Locate every Babesia divergens-infected red blood cell.
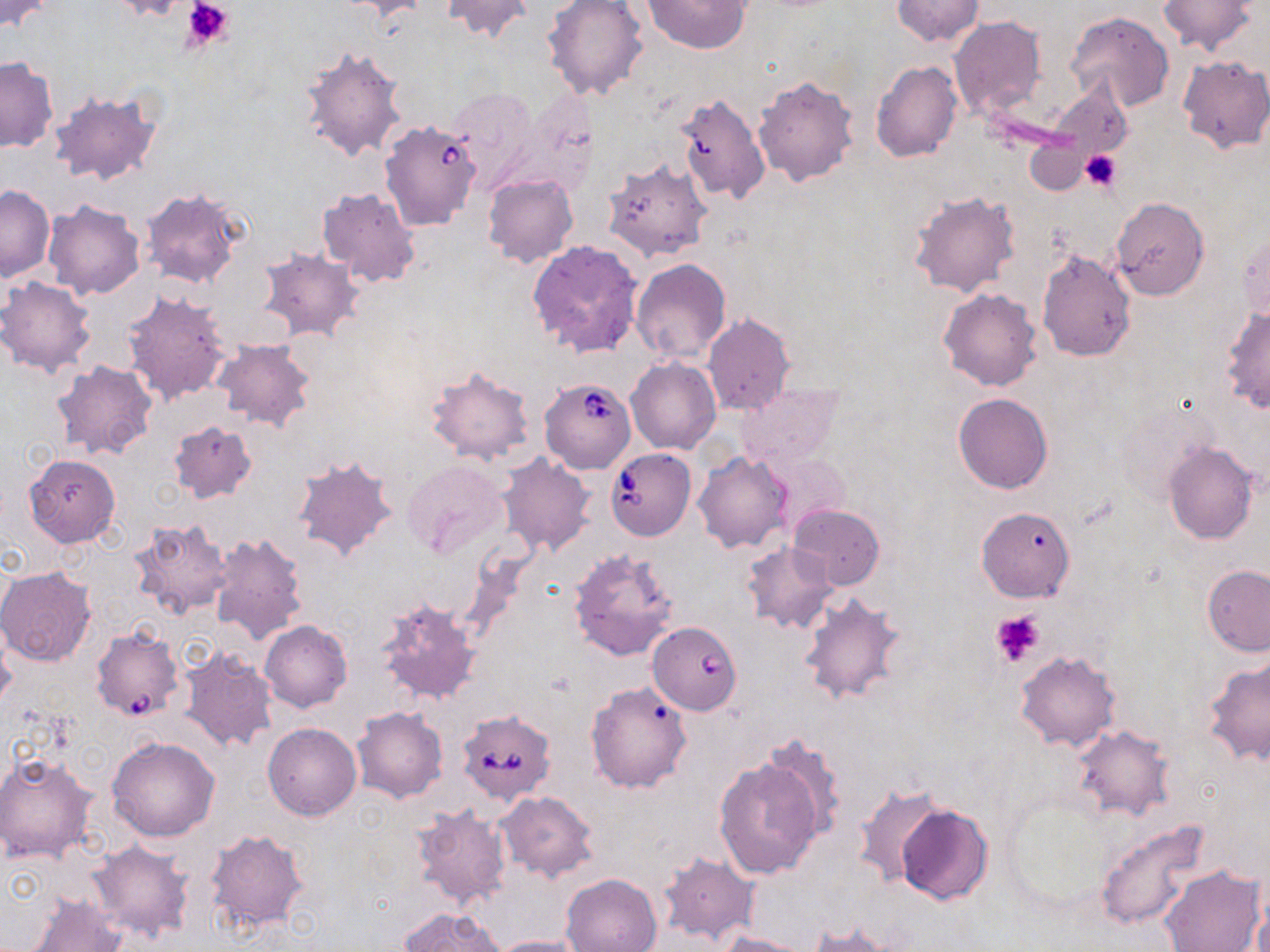

Approximate bounding boxes as (x1,y1)-(x2,y2) corner pairs in pixels.
Babesia divergens-infected red blood cells: (380,123)-(480,233), (539,378)-(636,472), (605,449)-(696,541), (648,623)-(742,722), (89,628)-(180,725), (456,710)-(556,804).

slide-level diagnosis = Babesia divergens
modality = optical microscopy
preparation = thin blood film
platelet locations = approximate bounding boxes as (x1,y1)-(x2,y2) corner pairs in pixels: (181,0)-(235,50), (1080,150)-(1121,191), (989,610)-(1045,668)
field of view = single
stain = May-Grünwald-Giemsa
uninfected red blood cell locations = approximate bounding boxes as (x1,y1)-(x2,y2) corner pairs in pixels: (0,0)-(54,32), (109,0)-(190,22), (341,0)-(430,20), (441,0)-(534,41), (544,0)-(650,104), (643,0)-(750,53), (892,0)-(983,46), (1157,0)-(1261,55), (1064,11)-(1175,111), (948,17)-(1047,120), (299,45)-(409,163), (1177,54)-(1270,155), (0,57)-(57,153), (871,61)-(962,163), (753,75)-(859,186), (1045,82)-(1132,165), (451,87)-(541,190), (48,89)-(161,188), (674,93)-(770,205), (1024,139)-(1091,194), (603,159)-(711,263), (484,175)-(578,268), (0,185)-(54,281), (139,187)-(244,289), (318,187)-(420,287), (909,192)-(1019,299), (1110,198)-(1210,299), (42,201)-(145,300), (1237,227)-(1269,325), (528,239)-(643,357), (255,247)-(365,343), (1036,250)-(1135,361), (631,259)-(730,363), (0,276)-(97,377), (938,288)-(1043,391), (121,290)-(233,406), (1222,304)-(1270,414), (703,313)-(794,416), (211,339)-(316,433), (626,359)-(720,455), (52,361)-(158,459), (425,366)-(536,468), (737,383)-(841,469), (953,393)-(1053,493), (1114,404)-(1214,506), (168,419)-(257,503), (1163,441)-(1257,544), (692,452)-(792,553), (23,453)-(120,547), (498,453)-(597,556), (759,454)-(851,534), (291,457)-(400,564), (400,461)-(509,561), (788,504)-(885,591), (976,506)-(1076,602), (128,519)-(232,621), (210,531)-(309,646), (742,543)-(838,633), (568,548)-(678,660), (1202,565)-(1270,655), (0,567)-(97,666), (797,592)-(906,708), (377,597)-(482,707), (260,620)-(352,711), (180,647)-(279,755), (1015,651)-(1121,752), (1202,655)-(1270,767), (585,681)-(695,794), (351,708)-(448,804), (263,723)-(361,821), (1070,724)-(1175,821), (758,735)-(847,841), (107,738)-(220,841), (0,754)-(99,865), (712,756)-(825,879), (851,782)-(946,889), (495,791)-(599,882), (895,803)-(993,904), (411,805)-(511,909), (1096,818)-(1213,929), (204,828)-(310,933), (87,839)-(194,943), (655,851)-(759,947), (1160,866)-(1266,952), (561,872)-(662,952), (27,893)-(128,952), (399,906)-(505,952), (804,923)-(904,951), (717,933)-(812,952), (486,935)-(591,952)
magnification = 1000x
image size = 1270×952 pixels